Report the malaria status of this cell.
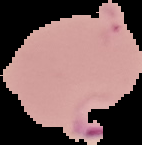

Parasitized.

image size = 142×145 pixels
preparation = thin blood smear
image type = segmented cell region with the area outside set to black